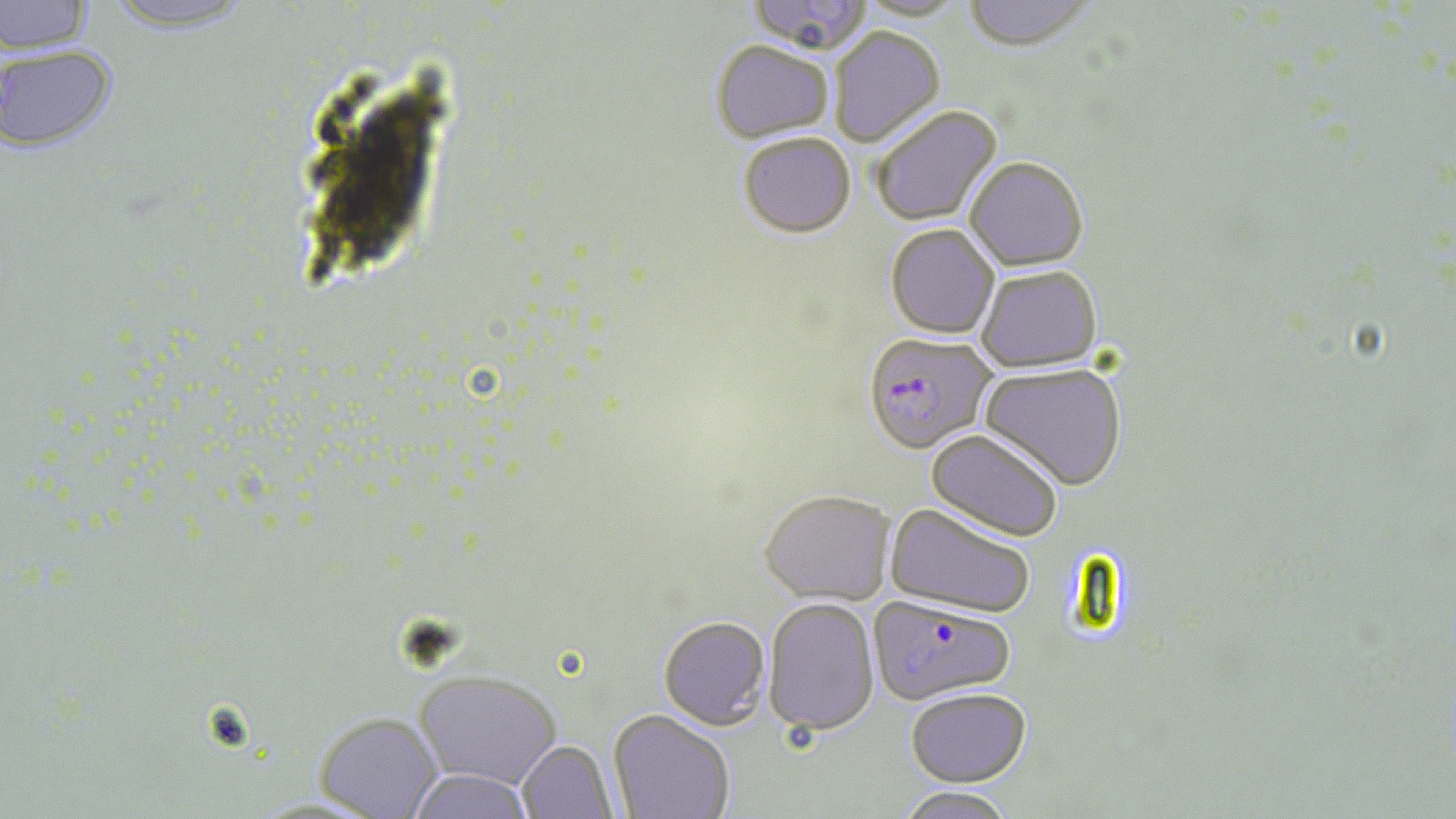
slide-level diagnosis = Plasmodium falciparum
uninfected red blood cell locations = approximate bounding boxes as (x1,y1)-(x2,y2) corner pairs in pixels: (0,0)-(97,57), (745,0)-(872,56), (855,0)-(969,23), (962,0)-(1098,54), (97,1)-(258,38), (829,28)-(945,148), (710,41)-(834,144), (0,47)-(119,156), (871,106)-(1003,227), (738,133)-(856,237), (965,157)-(1088,271), (885,224)-(1000,339), (975,265)-(1103,372), (979,363)-(1126,490), (926,428)-(1063,542), (760,489)-(896,605), (884,502)-(1037,618), (764,597)-(880,735), (658,615)-(771,729), (414,671)-(561,790), (905,687)-(1031,786), (608,710)-(735,819), (314,713)-(444,819), (517,741)-(618,819), (407,769)-(536,819), (896,786)-(1016,819)
modality = optical microscopy
Plasmodium falciparum-infected red blood cell locations = approximate bounding boxes as (x1,y1)-(x2,y2) corner pairs in pixels: (867,325)-(1003,454), (868,597)-(1016,705)
preparation = thin blood smear
magnification = 1000x
image size = 1456×819 pixels
field of view = single
stain = May-Grünwald-Giemsa